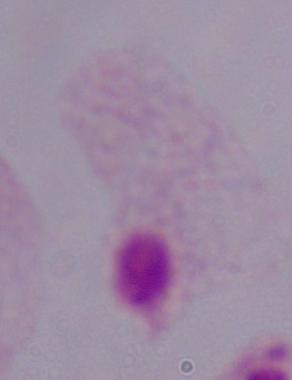
magnification = 1000x
modality = photomicrograph
identification = trichomonad